Give the position of every Plasmodium parasite.
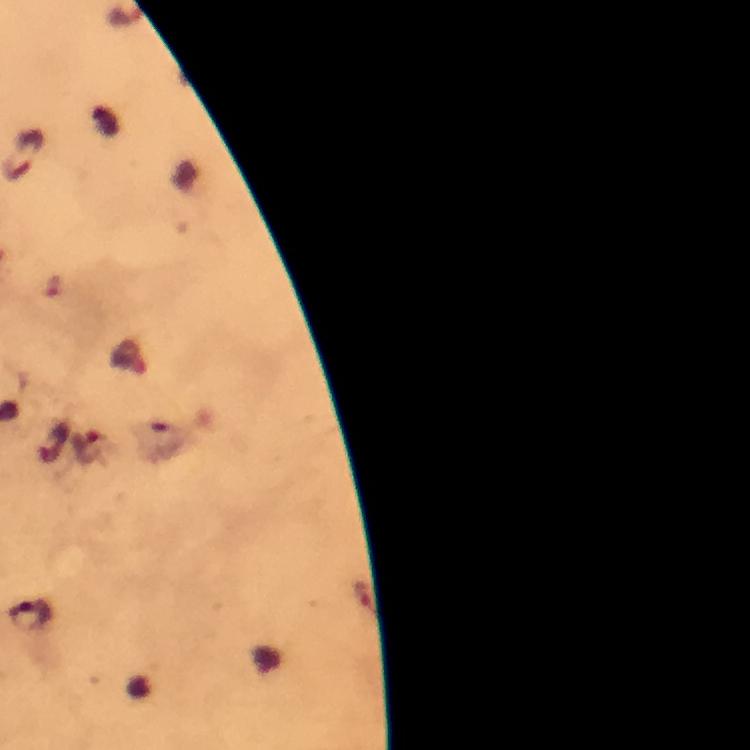

Approximate centers as (x, y) in pixels.
Plasmodium parasites: (90, 449), (28, 615).

Image is 750×750 pixels. 100x magnification. Giemsa-stained preparation. A crop from one field of view. Thick blood film. Photographed through the microscope with a smartphone camera. From a malaria diagnostic workup. Immersion oil applied.